State the blood parasite species.
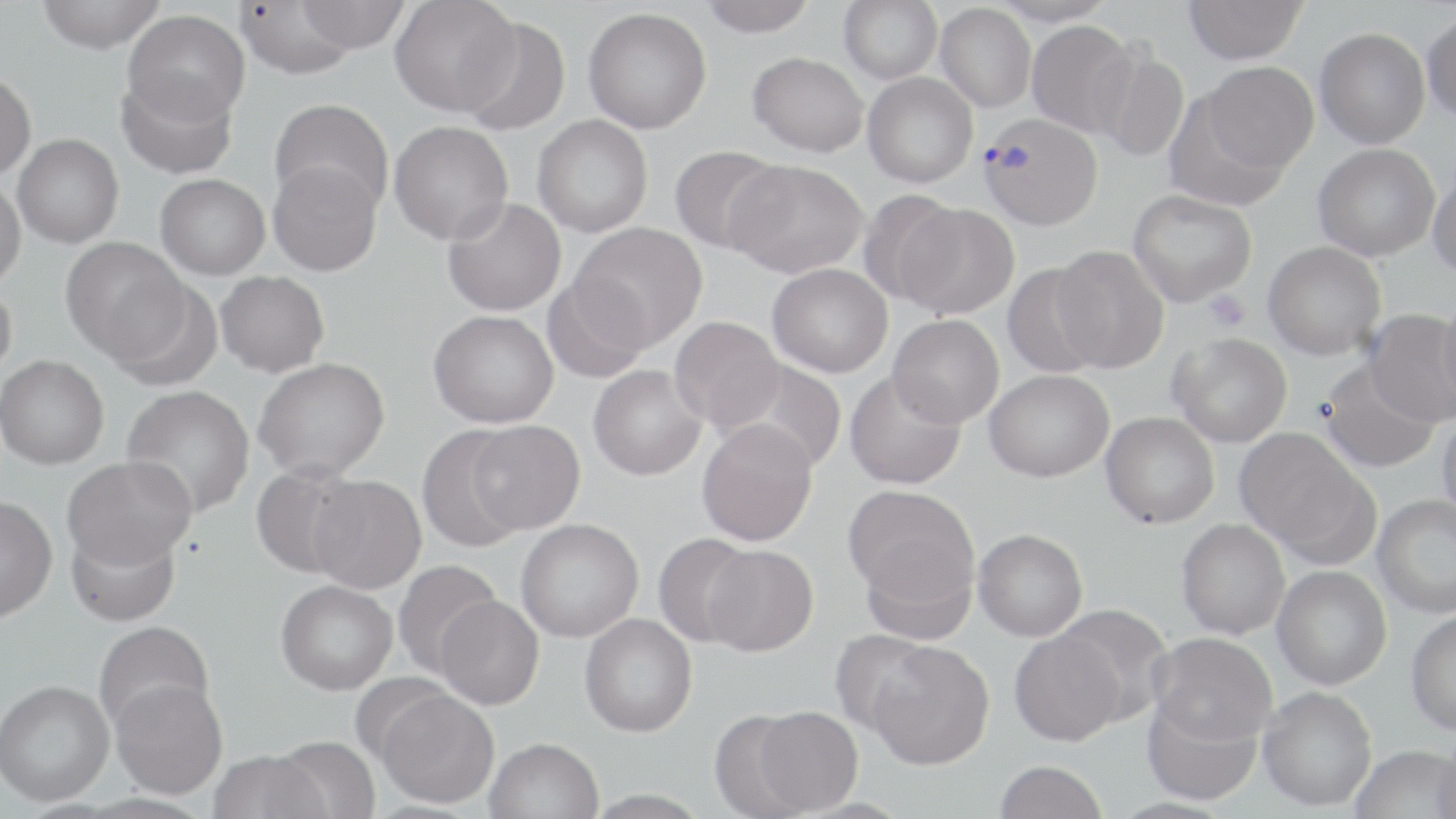

Plasmodium vivax.

field_of_view: one of a larger specimen
plasmodium_vivax_infected_red_blood_cell_locations: 'approximate bounding boxes as (x1, y1, x2, y2) in pixels: (978, 112, 1102, 229)'
magnification: 1000x
modality: optical microscopy
platelet_locations: 'approximate bounding boxes as (x1, y1, x2, y2) in pixels: (1203, 290, 1250, 332)'
preparation: thin blood smear
stain: May-Grünwald-Giemsa
image_size: 1456×819 pixels
uninfected_red_blood_cell_locations: 'approximate bounding boxes as (x1, y1, x2, y2) in pixels: (35, 0, 166, 54), (389, 0, 521, 117), (699, 0, 817, 37), (839, 0, 942, 84), (990, 0, 1118, 27), (1183, 0, 1307, 64), (233, 1, 362, 79), (294, 1, 409, 53), (935, 3, 1036, 112), (583, 7, 712, 134), (123, 10, 250, 126), (1421, 13, 1456, 123), (458, 16, 571, 136), (1026, 20, 1139, 137), (1314, 27, 1430, 149), (1095, 50, 1190, 163), (747, 51, 869, 157), (1202, 61, 1319, 173), (0, 69, 36, 181), (116, 71, 238, 180), (862, 72, 978, 188), (1164, 92, 1292, 211), (268, 98, 394, 215), (532, 115, 653, 237), (388, 121, 513, 245), (12, 134, 124, 248), (1312, 143, 1440, 261), (670, 144, 787, 255), (726, 159, 868, 278), (268, 161, 382, 276), (1428, 168, 1456, 279), (155, 174, 270, 280), (0, 179, 25, 291), (1127, 189, 1257, 307), (857, 190, 965, 305), (442, 197, 566, 316), (897, 203, 1020, 319), (572, 222, 707, 349), (60, 237, 188, 363), (1263, 241, 1386, 360), (1050, 244, 1169, 372), (1002, 262, 1107, 379), (767, 263, 893, 377), (215, 270, 329, 377), (542, 275, 651, 384), (108, 278, 223, 391), (0, 282, 17, 381), (1437, 298, 1456, 416), (1364, 309, 1456, 428), (428, 310, 559, 428), (887, 314, 1005, 428), (669, 316, 785, 432), (1168, 332, 1293, 447), (0, 355, 109, 470), (253, 357, 390, 481), (725, 359, 847, 473), (1320, 359, 1441, 474), (588, 365, 707, 481), (844, 369, 966, 490), (984, 369, 1114, 482), (120, 384, 255, 518), (1101, 411, 1220, 529), (1437, 412, 1456, 523), (696, 419, 818, 547), (467, 420, 585, 534), (416, 426, 530, 552), (1234, 428, 1372, 559), (62, 455, 196, 570), (250, 464, 363, 580), (308, 474, 426, 594), (842, 484, 980, 611), (1372, 495, 1456, 618), (0, 496, 57, 623), (516, 518, 644, 642), (1176, 518, 1291, 639), (65, 522, 181, 627), (973, 528, 1088, 641), (653, 533, 761, 647), (859, 539, 979, 645), (701, 544, 818, 656), (392, 560, 502, 679), (1272, 566, 1392, 690), (275, 580, 397, 695), (435, 595, 544, 710), (1051, 603, 1174, 725), (1406, 609, 1456, 735), (579, 613, 698, 737), (93, 621, 215, 735), (1009, 629, 1126, 746), (829, 631, 940, 736), (1148, 632, 1277, 746), (867, 641, 995, 770), (110, 677, 228, 799), (0, 679, 115, 806), (1258, 686, 1377, 811), (372, 687, 500, 809), (1141, 695, 1262, 806), (752, 706, 862, 814), (707, 709, 816, 819), (270, 735, 382, 819), (484, 737, 604, 819), (1433, 739, 1456, 819), (1350, 745, 1456, 819), (208, 750, 329, 819), (993, 759, 1108, 819)'